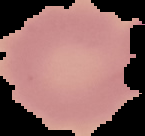 Segmented cell region on a black background. From a thin blood smear. Result: no Plasmodium parasites detected. Image is 145×136 pixels.